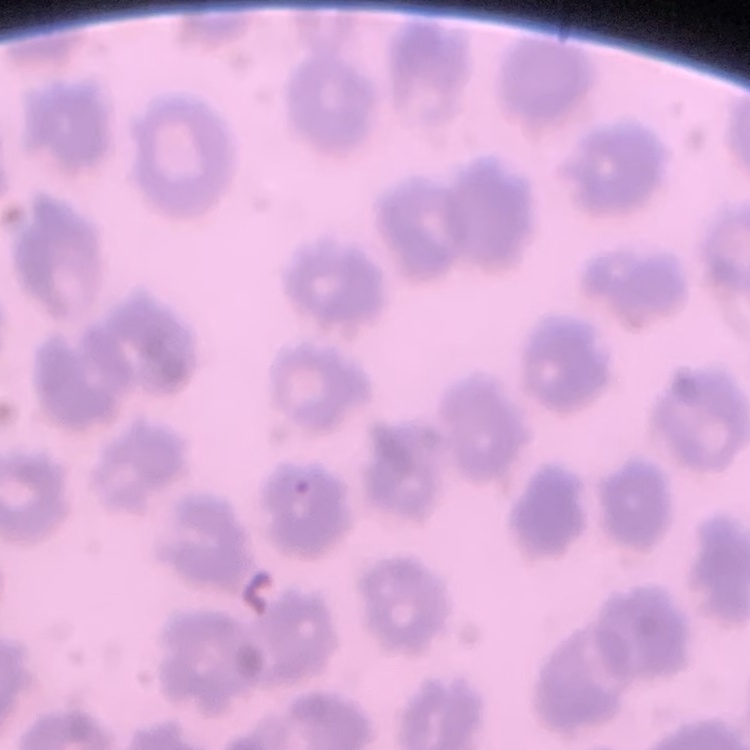

erythrocyte_morphology: no rouleaux formation
stain: Field's or Giemsa
image_type: square crop of a larger photomicrograph
preparation: thin blood smear